Assess this cell for malaria.
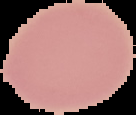

It is uninfected.

Image is 136×115 pixels. Cell region segmented out of the field of view; the surrounding area is masked to black. From a thin blood smear.